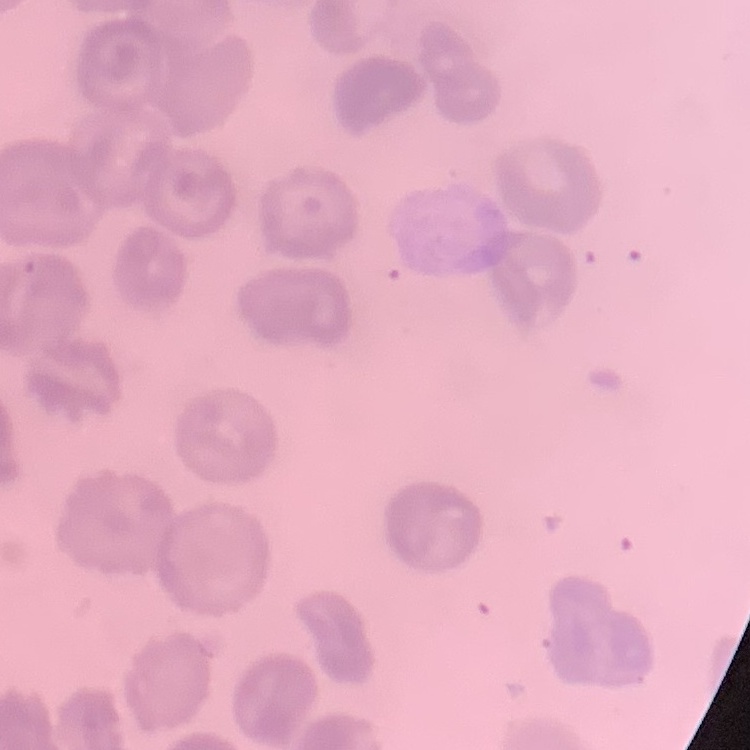

{
  "red_blood_cell_morphology": "no rouleaux formation",
  "image_type": "one tile cut from a larger photomicrograph",
  "stain": "Field's or Giemsa",
  "preparation": "thin peripheral smear"
}